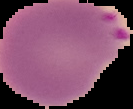

image type = segmented cell region on a black background
image size = 133×109 pixels
preparation = thin blood smear
malaria status = parasitized